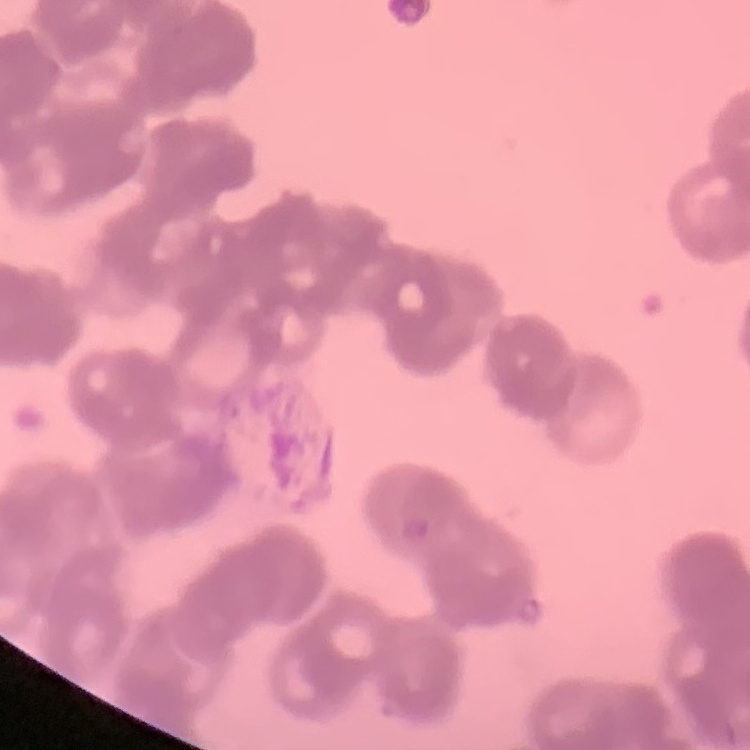

Summary:
  - Red blood cell morphology: rouleaux formation
  - Image type: one tile cut from a larger photomicrograph
  - Preparation: thin blood smear
  - Stain: Field's or Giemsa